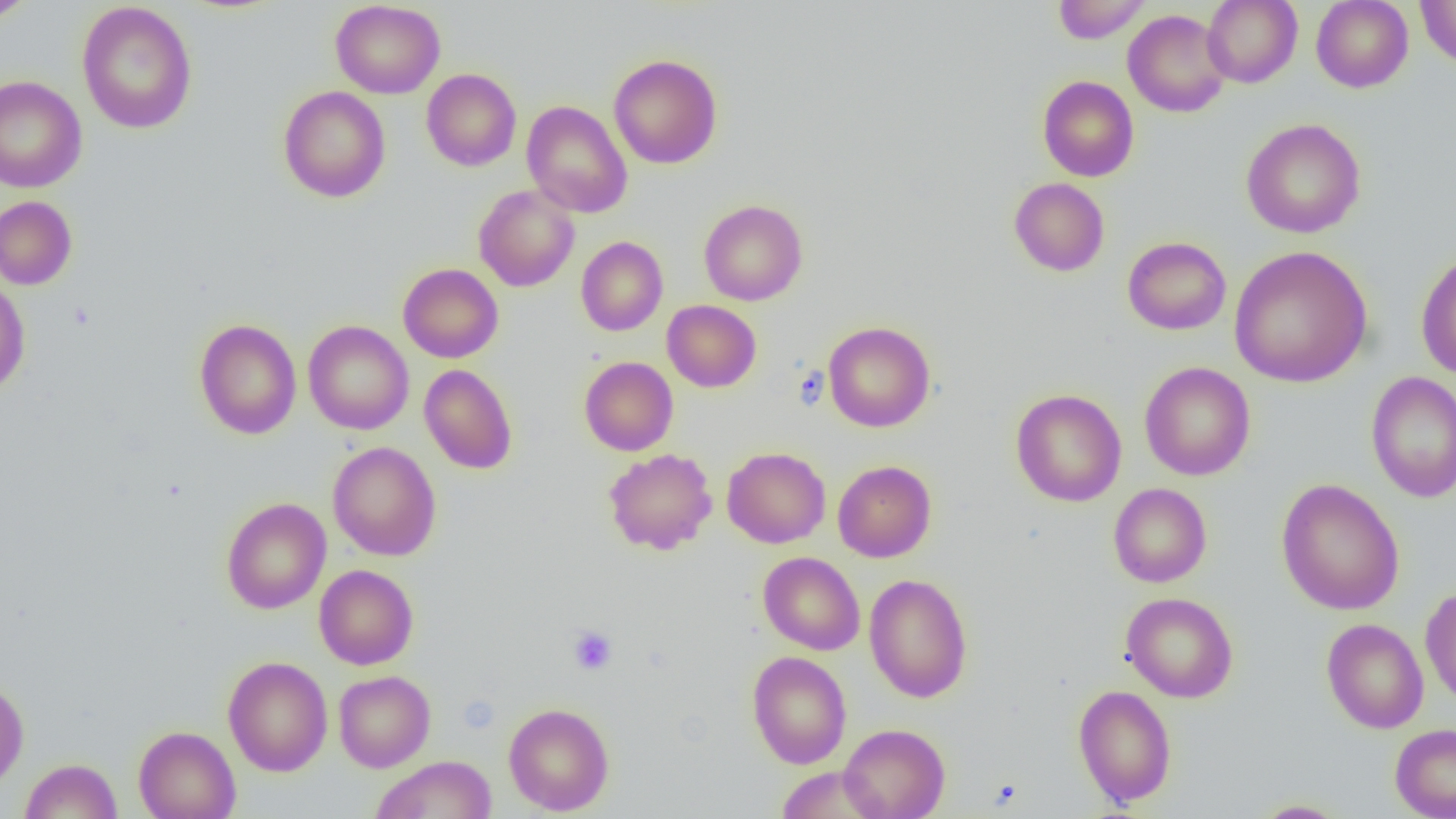 Approximate bounding boxes as named x1/y1/x2/y2 corners in pixels. Uninfected red blood cell locations: (x1=0, y1=0, x2=37, y2=25), (x1=1052, y1=0, x2=1151, y2=43), (x1=1202, y1=0, x2=1302, y2=87), (x1=1311, y1=0, x2=1413, y2=92), (x1=1416, y1=0, x2=1456, y2=70), (x1=331, y1=1, x2=445, y2=99), (x1=77, y1=2, x2=197, y2=134), (x1=1123, y1=10, x2=1231, y2=118), (x1=609, y1=53, x2=723, y2=169), (x1=421, y1=68, x2=521, y2=171), (x1=0, y1=76, x2=87, y2=193), (x1=1038, y1=76, x2=1138, y2=182), (x1=277, y1=85, x2=391, y2=202), (x1=521, y1=101, x2=633, y2=218), (x1=1241, y1=118, x2=1366, y2=238), (x1=1008, y1=177, x2=1110, y2=276), (x1=474, y1=185, x2=579, y2=292), (x1=0, y1=195, x2=77, y2=290), (x1=699, y1=200, x2=808, y2=305), (x1=576, y1=236, x2=668, y2=336), (x1=1122, y1=236, x2=1231, y2=335), (x1=1229, y1=246, x2=1373, y2=388), (x1=1415, y1=251, x2=1456, y2=380), (x1=398, y1=263, x2=503, y2=363), (x1=0, y1=278, x2=31, y2=396), (x1=662, y1=300, x2=761, y2=392), (x1=194, y1=319, x2=301, y2=439), (x1=303, y1=320, x2=414, y2=434), (x1=822, y1=321, x2=935, y2=432), (x1=579, y1=356, x2=678, y2=455), (x1=1139, y1=361, x2=1255, y2=480), (x1=419, y1=364, x2=518, y2=475), (x1=1366, y1=371, x2=1456, y2=503), (x1=1010, y1=389, x2=1127, y2=506), (x1=327, y1=441, x2=441, y2=561), (x1=722, y1=446, x2=831, y2=548), (x1=603, y1=448, x2=718, y2=555), (x1=833, y1=460, x2=937, y2=562), (x1=1276, y1=478, x2=1405, y2=615), (x1=1108, y1=483, x2=1212, y2=587), (x1=220, y1=497, x2=331, y2=614), (x1=758, y1=551, x2=865, y2=655), (x1=313, y1=565, x2=418, y2=670), (x1=864, y1=573, x2=973, y2=703), (x1=1420, y1=586, x2=1456, y2=707), (x1=1121, y1=592, x2=1238, y2=703), (x1=1321, y1=617, x2=1429, y2=734), (x1=748, y1=651, x2=851, y2=768), (x1=222, y1=656, x2=333, y2=776), (x1=333, y1=670, x2=435, y2=772), (x1=0, y1=678, x2=29, y2=790), (x1=1072, y1=685, x2=1177, y2=807), (x1=503, y1=702, x2=614, y2=815), (x1=1389, y1=723, x2=1456, y2=819), (x1=839, y1=724, x2=950, y2=818), (x1=133, y1=725, x2=241, y2=819), (x1=371, y1=755, x2=498, y2=819), (x1=20, y1=758, x2=122, y2=819), (x1=774, y1=768, x2=886, y2=817), (x1=1251, y1=799, x2=1351, y2=818). Platelet locations: (x1=793, y1=365, x2=829, y2=411), (x1=568, y1=625, x2=618, y2=675). Slide-level diagnosis: no evidence of blood parasites. One field of a larger specimen. Image is 1456×819 pixels. Captured at 1000x magnification. Thin blood film. Optical microscopy.